State which cell type is depicted.
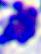

A leukocyte.

modality = photomicrograph
magnification = 400x